Identify the parasite.
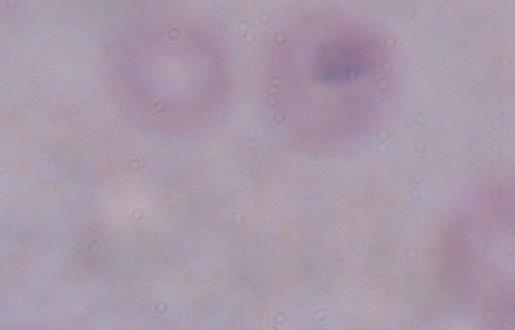
This is a trypanosome.

magnification: 1000x
modality: micrograph